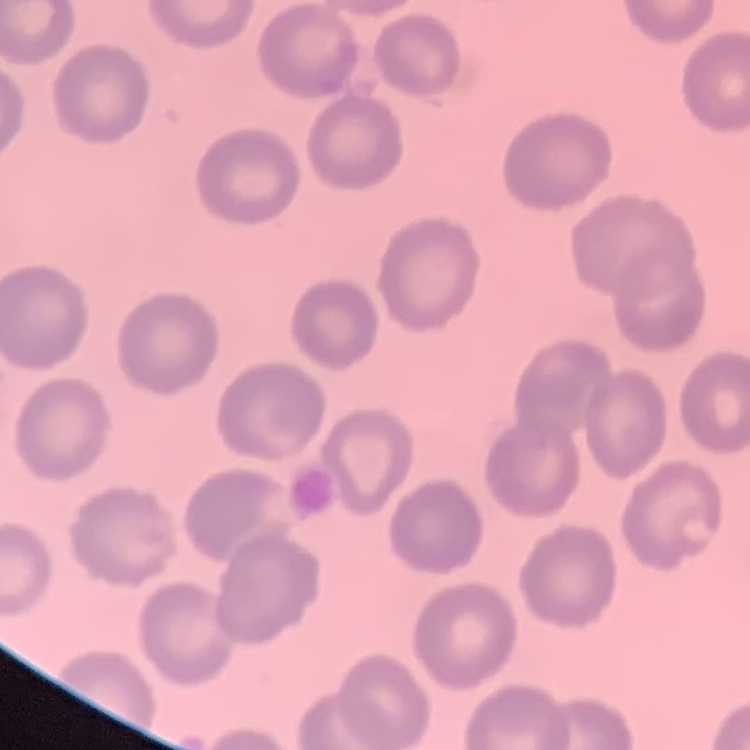 The erythrocytes show no rouleaux formation. Square crop of a larger photomicrograph. Thin blood film. Field's or Giemsa stain.